Report the malaria status of this cell.
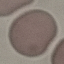
It is uninfected.

{
  "preparation": "thin blood film",
  "stain": "Giemsa",
  "capture": "smartphone through the microscope eyepiece",
  "image_type": "automatically extracted cell patch, resized to 64 × 64 pixels"
}